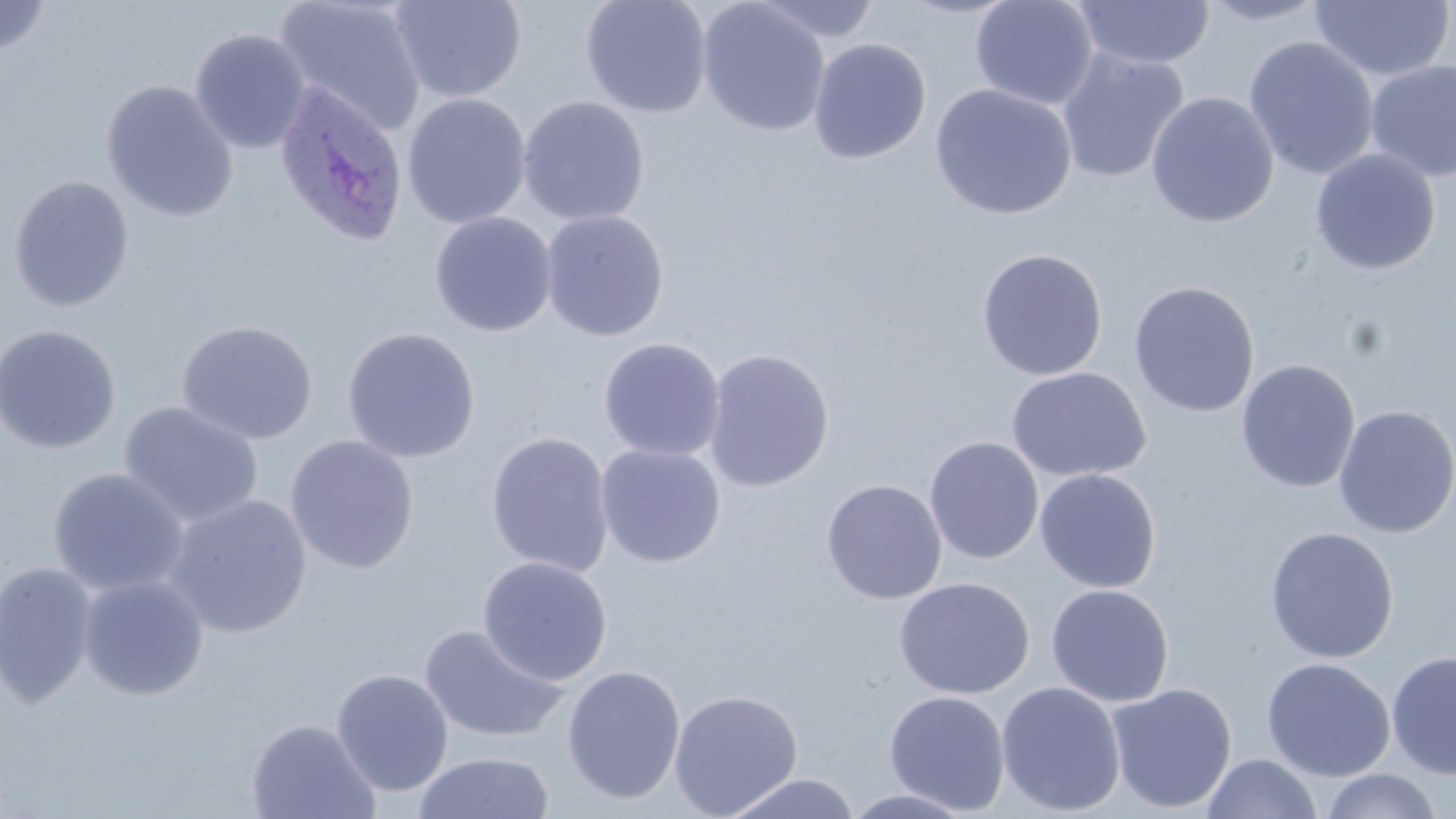 Approximate bounding boxes as [x1, y1, x2, y2] in pixels. Plasmodium ovale-infected red blood cell locations: [273, 78, 409, 247]. Uninfected red blood cell locations: [389, 0, 527, 104], [580, 0, 712, 118], [750, 0, 883, 43], [970, 0, 1099, 110], [1199, 0, 1330, 25], [0, 1, 52, 58], [274, 1, 428, 137], [696, 1, 831, 137], [1072, 1, 1215, 69], [1307, 1, 1455, 81], [189, 28, 310, 154], [1242, 35, 1380, 181], [808, 38, 932, 164], [1056, 49, 1190, 184], [1365, 59, 1456, 181], [100, 79, 238, 222], [929, 83, 1078, 220], [1145, 91, 1280, 228], [401, 93, 532, 229], [516, 95, 650, 227], [1310, 149, 1441, 275], [7, 175, 135, 312], [540, 209, 669, 342], [428, 211, 558, 337], [976, 248, 1108, 381], [1128, 280, 1261, 418], [176, 320, 318, 444], [0, 324, 122, 454], [342, 326, 481, 463], [598, 337, 726, 462], [702, 347, 835, 492], [1236, 359, 1360, 493], [1005, 366, 1152, 482], [118, 400, 264, 527], [1333, 404, 1456, 538], [485, 431, 615, 577], [284, 434, 420, 574], [924, 436, 1044, 564], [595, 443, 726, 568], [47, 467, 190, 596], [1034, 468, 1161, 593], [821, 478, 947, 604], [164, 493, 313, 638], [1264, 526, 1399, 664], [477, 555, 613, 686], [1, 560, 100, 709], [77, 574, 210, 700], [894, 576, 1035, 699], [1045, 584, 1175, 707], [419, 624, 568, 744], [1386, 650, 1456, 780], [1261, 657, 1396, 781], [561, 665, 686, 804], [331, 668, 454, 796], [996, 681, 1127, 816], [1106, 682, 1238, 814], [668, 689, 803, 818], [884, 690, 1011, 815], [245, 716, 381, 819], [413, 751, 556, 819], [1202, 752, 1321, 819], [1318, 769, 1444, 818], [722, 772, 862, 819], [840, 788, 979, 818]. Slide-level diagnosis: Plasmodium ovale. One field of a larger specimen. 1000x magnification. Image is 1456×819 pixels. Optical microscopy. May-Grünwald-Giemsa-stained preparation. Thin blood film.